Outline each blood parasite and name the species.
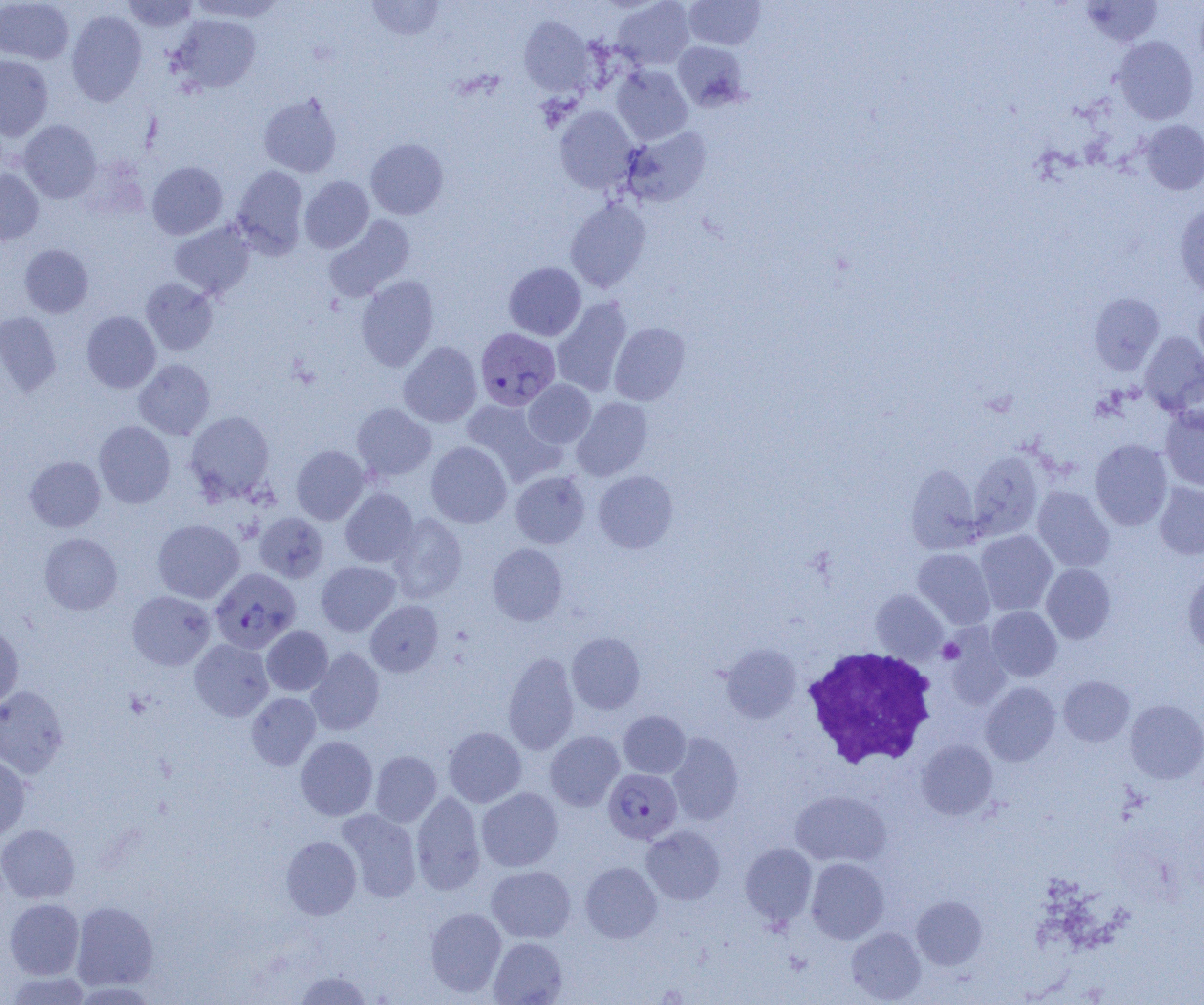
Approximate bounding boxes as named x1/y1/x2/y2 corners in pixels.
Plasmodium vivax-infected red blood cells: (x1=475, y1=327, x2=560, y2=411), (x1=210, y1=568, x2=300, y2=654), (x1=603, y1=768, x2=682, y2=844).
No Plasmodium falciparum, Plasmodium ovale, Plasmodium malariae, Babesia divergens, or Trypanosoma brucei observed.

slide-level diagnosis = Plasmodium vivax
preparation = thin blood film
platelet locations = approximate bounding boxes as named x1/y1/x2/y2 corners in pixels: (x1=938, y1=639, x2=964, y2=663)
magnification = 1000x
uninfected red blood cell locations = approximate bounding boxes as named x1/y1/x2/y2 corners in pixels: (x1=122, y1=0, x2=199, y2=33), (x1=187, y1=0, x2=287, y2=22), (x1=612, y1=0, x2=695, y2=69), (x1=683, y1=0, x2=765, y2=50), (x1=0, y1=1, x2=74, y2=64), (x1=367, y1=1, x2=445, y2=40), (x1=1082, y1=1, x2=1163, y2=47), (x1=66, y1=10, x2=147, y2=106), (x1=172, y1=14, x2=261, y2=93), (x1=519, y1=16, x2=595, y2=95), (x1=1113, y1=36, x2=1199, y2=124), (x1=673, y1=41, x2=748, y2=111), (x1=0, y1=55, x2=53, y2=141), (x1=611, y1=65, x2=693, y2=144), (x1=258, y1=92, x2=343, y2=178), (x1=555, y1=106, x2=638, y2=194), (x1=1140, y1=119, x2=1204, y2=195), (x1=18, y1=120, x2=101, y2=203), (x1=622, y1=127, x2=711, y2=207), (x1=365, y1=138, x2=448, y2=219), (x1=147, y1=161, x2=228, y2=239), (x1=232, y1=165, x2=308, y2=257), (x1=0, y1=169, x2=44, y2=245), (x1=300, y1=176, x2=374, y2=253), (x1=566, y1=198, x2=651, y2=293), (x1=1174, y1=203, x2=1204, y2=298), (x1=324, y1=216, x2=415, y2=301), (x1=169, y1=220, x2=255, y2=300), (x1=20, y1=244, x2=93, y2=317), (x1=504, y1=262, x2=586, y2=341), (x1=356, y1=276, x2=439, y2=371), (x1=140, y1=277, x2=217, y2=355), (x1=1089, y1=292, x2=1164, y2=374), (x1=1193, y1=293, x2=1204, y2=372), (x1=552, y1=297, x2=632, y2=397), (x1=81, y1=311, x2=161, y2=393), (x1=0, y1=312, x2=62, y2=397), (x1=609, y1=322, x2=690, y2=405), (x1=1140, y1=332, x2=1204, y2=415), (x1=399, y1=341, x2=482, y2=427), (x1=134, y1=359, x2=214, y2=440), (x1=523, y1=379, x2=596, y2=448), (x1=572, y1=397, x2=652, y2=480), (x1=461, y1=399, x2=557, y2=482), (x1=352, y1=403, x2=436, y2=480), (x1=1160, y1=407, x2=1204, y2=490), (x1=185, y1=410, x2=275, y2=502), (x1=94, y1=420, x2=175, y2=508), (x1=1090, y1=439, x2=1172, y2=530), (x1=426, y1=441, x2=512, y2=528), (x1=291, y1=445, x2=369, y2=524), (x1=968, y1=450, x2=1044, y2=539), (x1=25, y1=456, x2=106, y2=532), (x1=906, y1=464, x2=982, y2=553), (x1=510, y1=470, x2=590, y2=548), (x1=593, y1=470, x2=678, y2=553), (x1=1154, y1=482, x2=1204, y2=560), (x1=1032, y1=486, x2=1114, y2=571), (x1=340, y1=487, x2=418, y2=567), (x1=254, y1=512, x2=329, y2=583), (x1=387, y1=512, x2=467, y2=603), (x1=152, y1=519, x2=244, y2=604), (x1=975, y1=530, x2=1057, y2=615), (x1=39, y1=532, x2=122, y2=615), (x1=487, y1=543, x2=567, y2=625), (x1=913, y1=548, x2=995, y2=629), (x1=316, y1=561, x2=400, y2=636), (x1=1041, y1=563, x2=1116, y2=643), (x1=1182, y1=571, x2=1204, y2=657), (x1=871, y1=589, x2=948, y2=663), (x1=127, y1=590, x2=215, y2=670), (x1=365, y1=600, x2=443, y2=676), (x1=986, y1=606, x2=1061, y2=681), (x1=0, y1=620, x2=23, y2=710), (x1=262, y1=625, x2=333, y2=695), (x1=567, y1=633, x2=645, y2=714), (x1=190, y1=639, x2=273, y2=721), (x1=721, y1=644, x2=801, y2=723), (x1=306, y1=647, x2=385, y2=735), (x1=502, y1=651, x2=580, y2=755), (x1=1058, y1=675, x2=1135, y2=747), (x1=981, y1=682, x2=1060, y2=766), (x1=0, y1=685, x2=68, y2=778), (x1=246, y1=692, x2=320, y2=770), (x1=1125, y1=700, x2=1204, y2=784), (x1=618, y1=710, x2=690, y2=778), (x1=443, y1=726, x2=526, y2=807), (x1=545, y1=730, x2=624, y2=811), (x1=667, y1=733, x2=744, y2=825), (x1=296, y1=736, x2=378, y2=820), (x1=916, y1=740, x2=997, y2=820), (x1=370, y1=750, x2=442, y2=827), (x1=0, y1=756, x2=31, y2=841), (x1=476, y1=787, x2=563, y2=871), (x1=790, y1=790, x2=891, y2=867), (x1=411, y1=792, x2=486, y2=894), (x1=336, y1=809, x2=422, y2=902), (x1=0, y1=824, x2=80, y2=903), (x1=641, y1=826, x2=725, y2=904), (x1=281, y1=835, x2=361, y2=919), (x1=740, y1=843, x2=817, y2=926), (x1=806, y1=857, x2=889, y2=943), (x1=580, y1=862, x2=662, y2=943), (x1=486, y1=865, x2=576, y2=942), (x1=911, y1=896, x2=987, y2=969), (x1=4, y1=898, x2=85, y2=979), (x1=72, y1=901, x2=158, y2=991), (x1=425, y1=907, x2=506, y2=996), (x1=846, y1=927, x2=926, y2=1003), (x1=489, y1=937, x2=568, y2=1004), (x1=292, y1=970, x2=374, y2=1004), (x1=5, y1=971, x2=91, y2=1004)
white blood cell locations = approximate bounding boxes as named x1/y1/x2/y2 corners in pixels: (x1=802, y1=646, x2=938, y2=770)
modality = light microscopy
image size = 1204×1005 pixels
field of view = one of a larger specimen